Name the parasite shown.
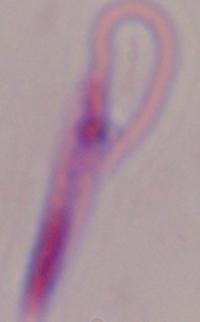

Leishmania.

{
  "modality": "photomicrograph",
  "magnification": "1000x"
}